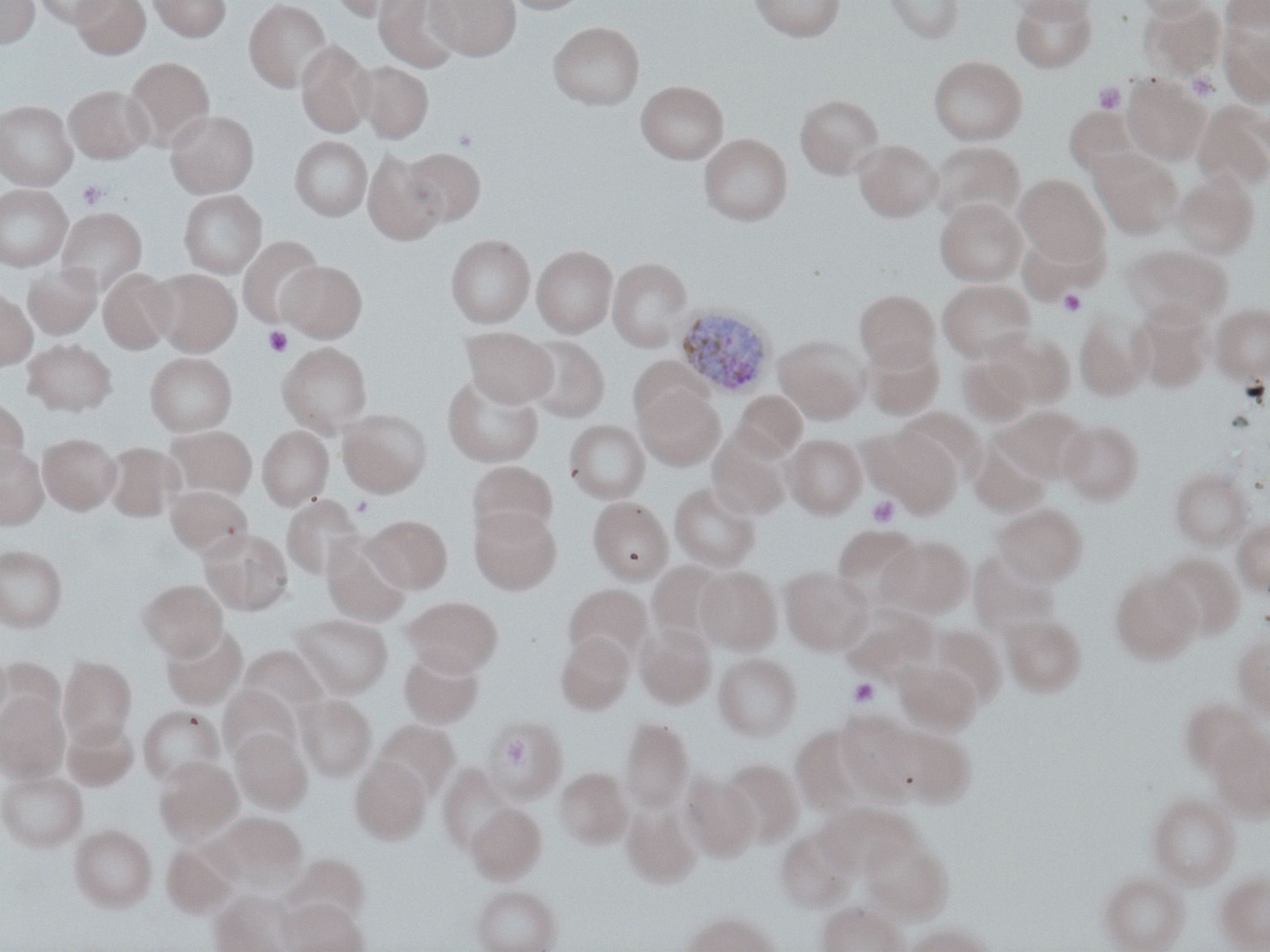

Approximate bounding boxes as named x1/y1/x2/y2 corners in pixels. Platelet locations: (x1=1186, y1=72, x2=1218, y2=100), (x1=1094, y1=82, x2=1127, y2=114), (x1=77, y1=180, x2=108, y2=209), (x1=1058, y1=289, x2=1087, y2=316), (x1=263, y1=325, x2=293, y2=358), (x1=867, y1=495, x2=900, y2=528), (x1=352, y1=496, x2=373, y2=517), (x1=847, y1=678, x2=880, y2=707). Uninfected red blood cell locations: (x1=0, y1=0, x2=39, y2=49), (x1=32, y1=0, x2=117, y2=27), (x1=71, y1=0, x2=150, y2=60), (x1=148, y1=0, x2=231, y2=42), (x1=243, y1=0, x2=332, y2=92), (x1=330, y1=0, x2=416, y2=22), (x1=373, y1=0, x2=461, y2=72), (x1=426, y1=0, x2=520, y2=60), (x1=504, y1=0, x2=590, y2=14), (x1=749, y1=0, x2=846, y2=41), (x1=884, y1=0, x2=964, y2=43), (x1=1009, y1=0, x2=1096, y2=21), (x1=1010, y1=0, x2=1097, y2=72), (x1=1134, y1=0, x2=1211, y2=19), (x1=1221, y1=0, x2=1269, y2=42), (x1=1141, y1=1, x2=1226, y2=79), (x1=547, y1=21, x2=645, y2=110), (x1=1219, y1=22, x2=1270, y2=107), (x1=296, y1=40, x2=375, y2=137), (x1=929, y1=55, x2=1028, y2=145), (x1=124, y1=56, x2=214, y2=151), (x1=354, y1=60, x2=433, y2=143), (x1=1122, y1=75, x2=1209, y2=165), (x1=635, y1=80, x2=728, y2=164), (x1=64, y1=84, x2=152, y2=164), (x1=795, y1=94, x2=885, y2=178), (x1=0, y1=100, x2=77, y2=190), (x1=1192, y1=100, x2=1270, y2=191), (x1=1064, y1=106, x2=1140, y2=176), (x1=165, y1=109, x2=259, y2=197), (x1=698, y1=134, x2=793, y2=225), (x1=290, y1=136, x2=371, y2=220), (x1=854, y1=140, x2=943, y2=221), (x1=931, y1=141, x2=1025, y2=225), (x1=400, y1=147, x2=485, y2=227), (x1=1089, y1=147, x2=1182, y2=238), (x1=362, y1=149, x2=447, y2=246), (x1=1172, y1=172, x2=1258, y2=258), (x1=1015, y1=174, x2=1107, y2=265), (x1=0, y1=184, x2=73, y2=272), (x1=178, y1=190, x2=267, y2=278), (x1=935, y1=199, x2=1028, y2=286), (x1=56, y1=208, x2=147, y2=295), (x1=446, y1=234, x2=534, y2=327), (x1=238, y1=235, x2=324, y2=327), (x1=532, y1=244, x2=618, y2=337), (x1=1123, y1=244, x2=1232, y2=327), (x1=608, y1=258, x2=692, y2=350), (x1=279, y1=261, x2=367, y2=341), (x1=23, y1=264, x2=101, y2=339), (x1=98, y1=268, x2=177, y2=353), (x1=150, y1=269, x2=241, y2=356), (x1=937, y1=279, x2=1036, y2=362), (x1=854, y1=289, x2=940, y2=370), (x1=0, y1=290, x2=37, y2=370), (x1=1211, y1=303, x2=1270, y2=383), (x1=1131, y1=306, x2=1212, y2=392), (x1=1074, y1=311, x2=1151, y2=401), (x1=463, y1=327, x2=557, y2=407), (x1=987, y1=328, x2=1075, y2=407), (x1=774, y1=334, x2=869, y2=424), (x1=522, y1=336, x2=610, y2=422), (x1=21, y1=338, x2=117, y2=416), (x1=863, y1=340, x2=944, y2=420), (x1=276, y1=342, x2=372, y2=435), (x1=145, y1=353, x2=237, y2=436), (x1=627, y1=356, x2=711, y2=431), (x1=958, y1=356, x2=1032, y2=424), (x1=442, y1=375, x2=544, y2=467), (x1=636, y1=384, x2=724, y2=470), (x1=733, y1=390, x2=807, y2=460), (x1=0, y1=398, x2=29, y2=478), (x1=995, y1=406, x2=1088, y2=481), (x1=899, y1=407, x2=987, y2=483), (x1=338, y1=408, x2=432, y2=496), (x1=564, y1=419, x2=650, y2=504), (x1=1058, y1=419, x2=1145, y2=504), (x1=165, y1=425, x2=257, y2=502), (x1=258, y1=425, x2=333, y2=510), (x1=868, y1=427, x2=961, y2=516), (x1=38, y1=430, x2=121, y2=515), (x1=708, y1=432, x2=792, y2=520), (x1=784, y1=433, x2=866, y2=518), (x1=969, y1=439, x2=1050, y2=515), (x1=102, y1=442, x2=182, y2=523), (x1=0, y1=444, x2=48, y2=529), (x1=466, y1=461, x2=558, y2=542), (x1=1170, y1=468, x2=1252, y2=550), (x1=669, y1=482, x2=760, y2=572), (x1=166, y1=485, x2=253, y2=559), (x1=282, y1=495, x2=364, y2=580), (x1=588, y1=497, x2=672, y2=582), (x1=993, y1=503, x2=1088, y2=586), (x1=469, y1=504, x2=561, y2=594), (x1=363, y1=514, x2=452, y2=592), (x1=1233, y1=519, x2=1270, y2=596), (x1=832, y1=523, x2=926, y2=610), (x1=199, y1=528, x2=293, y2=616), (x1=321, y1=533, x2=412, y2=626), (x1=877, y1=535, x2=973, y2=619), (x1=0, y1=545, x2=67, y2=632), (x1=1158, y1=553, x2=1246, y2=640), (x1=647, y1=561, x2=727, y2=644), (x1=780, y1=565, x2=873, y2=655), (x1=695, y1=566, x2=781, y2=653), (x1=1111, y1=571, x2=1202, y2=663), (x1=137, y1=579, x2=227, y2=660), (x1=563, y1=584, x2=652, y2=665), (x1=404, y1=596, x2=502, y2=676), (x1=842, y1=606, x2=938, y2=682), (x1=292, y1=613, x2=393, y2=699), (x1=1002, y1=613, x2=1087, y2=697), (x1=161, y1=624, x2=249, y2=710), (x1=636, y1=624, x2=715, y2=708), (x1=928, y1=625, x2=1007, y2=708), (x1=555, y1=633, x2=634, y2=715), (x1=1232, y1=634, x2=1270, y2=718), (x1=237, y1=644, x2=330, y2=721), (x1=399, y1=649, x2=484, y2=728), (x1=713, y1=653, x2=802, y2=741), (x1=59, y1=655, x2=137, y2=745), (x1=895, y1=661, x2=982, y2=735), (x1=219, y1=685, x2=301, y2=762), (x1=0, y1=692, x2=70, y2=781), (x1=294, y1=695, x2=377, y2=781), (x1=1180, y1=699, x2=1259, y2=776), (x1=139, y1=706, x2=225, y2=784), (x1=835, y1=710, x2=917, y2=796), (x1=620, y1=717, x2=693, y2=813), (x1=62, y1=718, x2=138, y2=790), (x1=482, y1=718, x2=567, y2=802), (x1=373, y1=720, x2=460, y2=799), (x1=878, y1=723, x2=975, y2=807), (x1=790, y1=725, x2=867, y2=812), (x1=230, y1=728, x2=312, y2=812), (x1=1210, y1=729, x2=1270, y2=820), (x1=154, y1=756, x2=243, y2=843), (x1=349, y1=757, x2=431, y2=844), (x1=720, y1=759, x2=804, y2=846), (x1=437, y1=764, x2=513, y2=854), (x1=555, y1=767, x2=633, y2=848), (x1=0, y1=768, x2=87, y2=852), (x1=681, y1=773, x2=761, y2=861), (x1=1147, y1=791, x2=1239, y2=888), (x1=466, y1=803, x2=546, y2=883), (x1=818, y1=803, x2=908, y2=875), (x1=622, y1=804, x2=701, y2=888), (x1=206, y1=813, x2=307, y2=891), (x1=69, y1=824, x2=157, y2=912), (x1=775, y1=829, x2=853, y2=913), (x1=861, y1=829, x2=952, y2=921), (x1=162, y1=843, x2=237, y2=918), (x1=282, y1=853, x2=370, y2=926), (x1=1099, y1=871, x2=1189, y2=952), (x1=1216, y1=871, x2=1270, y2=952), (x1=471, y1=884, x2=562, y2=952), (x1=209, y1=891, x2=296, y2=952), (x1=281, y1=898, x2=369, y2=952), (x1=818, y1=901, x2=906, y2=952), (x1=681, y1=910, x2=780, y2=952), (x1=902, y1=923, x2=997, y2=952). Plasmodium ovale-infected red blood cell locations: (x1=674, y1=303, x2=777, y2=398). Slide-level diagnosis: Plasmodium ovale. Thin blood film. Image is 1270×952 pixels. Captured at 1000x magnification. Single field of view. Optical microscopy. May-Grünwald-Giemsa-stained preparation.